Locate every blood parasite and identify its species.
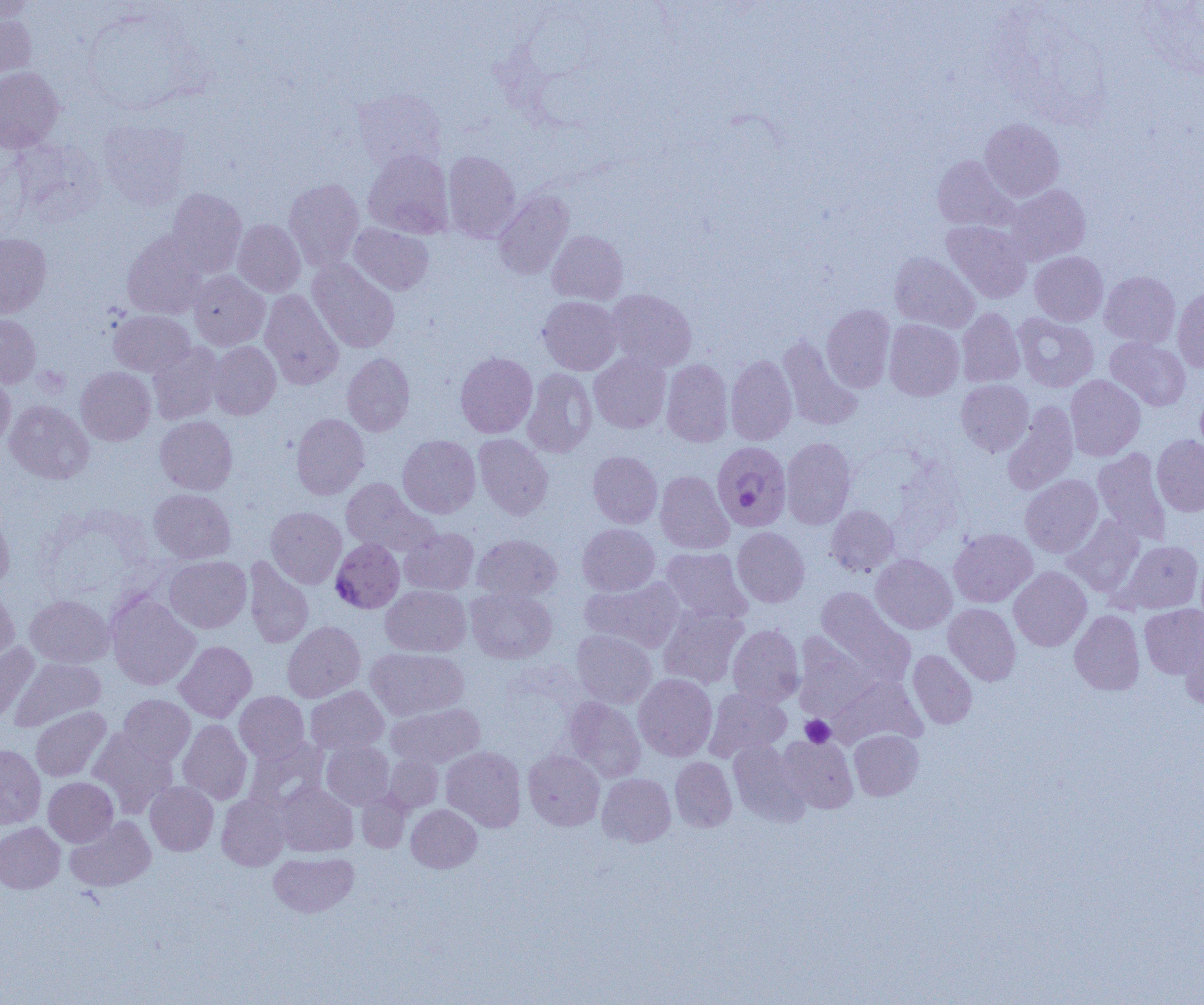

Approximate bounding boxes as named x1/y1/x2/y2 corners in pixels.
Plasmodium falciparum-infected red blood cells: (x1=711, y1=441, x2=791, y2=531), (x1=328, y1=540, x2=408, y2=614).
No Plasmodium ovale, Plasmodium malariae, Plasmodium vivax, Babesia divergens, or Trypanosoma brucei observed.

Uninfected red blood cell locations: (x1=0, y1=0, x2=36, y2=22), (x1=0, y1=9, x2=36, y2=83), (x1=0, y1=67, x2=63, y2=152), (x1=352, y1=89, x2=447, y2=173), (x1=98, y1=117, x2=192, y2=209), (x1=979, y1=118, x2=1064, y2=201), (x1=10, y1=138, x2=106, y2=225), (x1=363, y1=149, x2=454, y2=238), (x1=442, y1=151, x2=521, y2=242), (x1=932, y1=155, x2=1018, y2=231), (x1=284, y1=178, x2=364, y2=271), (x1=1005, y1=185, x2=1091, y2=264), (x1=167, y1=187, x2=247, y2=277), (x1=493, y1=190, x2=574, y2=280), (x1=233, y1=219, x2=305, y2=297), (x1=941, y1=221, x2=1032, y2=303), (x1=349, y1=223, x2=433, y2=295), (x1=547, y1=230, x2=628, y2=304), (x1=122, y1=231, x2=208, y2=319), (x1=0, y1=233, x2=51, y2=317), (x1=1030, y1=251, x2=1108, y2=326), (x1=889, y1=252, x2=980, y2=333), (x1=307, y1=259, x2=399, y2=353), (x1=188, y1=270, x2=270, y2=350), (x1=1099, y1=271, x2=1180, y2=348), (x1=1172, y1=287, x2=1204, y2=373), (x1=260, y1=289, x2=344, y2=389), (x1=606, y1=289, x2=697, y2=371), (x1=538, y1=296, x2=622, y2=375), (x1=821, y1=304, x2=895, y2=392), (x1=957, y1=308, x2=1025, y2=387), (x1=109, y1=310, x2=195, y2=376), (x1=1013, y1=313, x2=1098, y2=392), (x1=0, y1=314, x2=41, y2=387), (x1=884, y1=319, x2=964, y2=401), (x1=778, y1=336, x2=862, y2=431), (x1=1105, y1=337, x2=1191, y2=411), (x1=208, y1=341, x2=281, y2=419), (x1=148, y1=343, x2=225, y2=425), (x1=455, y1=352, x2=537, y2=438), (x1=589, y1=352, x2=671, y2=433), (x1=342, y1=353, x2=414, y2=436), (x1=726, y1=355, x2=797, y2=445), (x1=661, y1=359, x2=733, y2=446), (x1=76, y1=367, x2=155, y2=445), (x1=522, y1=368, x2=597, y2=457), (x1=0, y1=373, x2=15, y2=449), (x1=1065, y1=375, x2=1146, y2=460), (x1=956, y1=380, x2=1033, y2=456), (x1=1195, y1=387, x2=1204, y2=461), (x1=4, y1=400, x2=94, y2=484), (x1=1002, y1=402, x2=1078, y2=494), (x1=291, y1=413, x2=369, y2=499), (x1=155, y1=416, x2=237, y2=495), (x1=474, y1=434, x2=553, y2=520), (x1=397, y1=435, x2=481, y2=518), (x1=1152, y1=435, x2=1204, y2=517), (x1=780, y1=437, x2=856, y2=529), (x1=1093, y1=448, x2=1171, y2=542), (x1=588, y1=451, x2=662, y2=528), (x1=655, y1=471, x2=734, y2=554), (x1=1020, y1=474, x2=1103, y2=557), (x1=341, y1=478, x2=436, y2=556), (x1=149, y1=488, x2=235, y2=563), (x1=265, y1=506, x2=346, y2=587), (x1=826, y1=506, x2=899, y2=576), (x1=0, y1=509, x2=14, y2=592), (x1=1062, y1=516, x2=1145, y2=596), (x1=578, y1=524, x2=660, y2=596), (x1=400, y1=527, x2=479, y2=595), (x1=732, y1=527, x2=809, y2=607), (x1=949, y1=528, x2=1036, y2=607), (x1=472, y1=534, x2=561, y2=602), (x1=1119, y1=541, x2=1203, y2=613), (x1=661, y1=547, x2=752, y2=624), (x1=1196, y1=551, x2=1204, y2=628), (x1=871, y1=554, x2=957, y2=634), (x1=164, y1=556, x2=251, y2=632), (x1=243, y1=557, x2=313, y2=648), (x1=1009, y1=566, x2=1091, y2=651), (x1=581, y1=577, x2=684, y2=652), (x1=380, y1=585, x2=470, y2=656), (x1=0, y1=587, x2=19, y2=669), (x1=466, y1=587, x2=557, y2=663), (x1=816, y1=587, x2=915, y2=683), (x1=107, y1=592, x2=200, y2=690), (x1=25, y1=594, x2=113, y2=667), (x1=943, y1=603, x2=1021, y2=686), (x1=1139, y1=604, x2=1204, y2=678), (x1=658, y1=606, x2=748, y2=689), (x1=1070, y1=610, x2=1144, y2=695), (x1=282, y1=621, x2=365, y2=702), (x1=727, y1=625, x2=805, y2=706), (x1=1181, y1=627, x2=1204, y2=710), (x1=571, y1=629, x2=657, y2=708), (x1=793, y1=633, x2=880, y2=719), (x1=174, y1=640, x2=256, y2=722), (x1=0, y1=643, x2=39, y2=725), (x1=366, y1=647, x2=468, y2=720), (x1=908, y1=650, x2=977, y2=728), (x1=12, y1=657, x2=106, y2=731), (x1=634, y1=674, x2=717, y2=761), (x1=829, y1=675, x2=925, y2=748), (x1=305, y1=685, x2=388, y2=755), (x1=703, y1=687, x2=791, y2=761), (x1=235, y1=691, x2=309, y2=762), (x1=118, y1=695, x2=195, y2=766), (x1=563, y1=697, x2=645, y2=782), (x1=387, y1=703, x2=485, y2=768), (x1=30, y1=706, x2=110, y2=781), (x1=178, y1=720, x2=252, y2=805), (x1=89, y1=728, x2=177, y2=817), (x1=849, y1=729, x2=923, y2=800), (x1=778, y1=734, x2=858, y2=813), (x1=243, y1=737, x2=328, y2=814), (x1=322, y1=740, x2=394, y2=809), (x1=728, y1=740, x2=808, y2=825), (x1=0, y1=744, x2=45, y2=828), (x1=441, y1=746, x2=526, y2=832), (x1=523, y1=750, x2=604, y2=830), (x1=383, y1=754, x2=442, y2=812), (x1=670, y1=757, x2=737, y2=831), (x1=597, y1=773, x2=675, y2=847), (x1=44, y1=777, x2=118, y2=846), (x1=145, y1=781, x2=218, y2=855), (x1=275, y1=781, x2=358, y2=856), (x1=356, y1=790, x2=411, y2=852), (x1=216, y1=794, x2=289, y2=870), (x1=406, y1=804, x2=482, y2=872), (x1=65, y1=816, x2=155, y2=892), (x1=0, y1=822, x2=65, y2=893), (x1=269, y1=852, x2=358, y2=917). Platelet locations: (x1=800, y1=715, x2=835, y2=747). Slide-level diagnosis: Plasmodium falciparum. Single field of view. Captured at 1000x magnification. Thin blood smear. Light microscopy. Image is 1204×1005 pixels.